Locate the cells, classifying each as a parasitized RBC, an uninfected RBC, or a WBC.
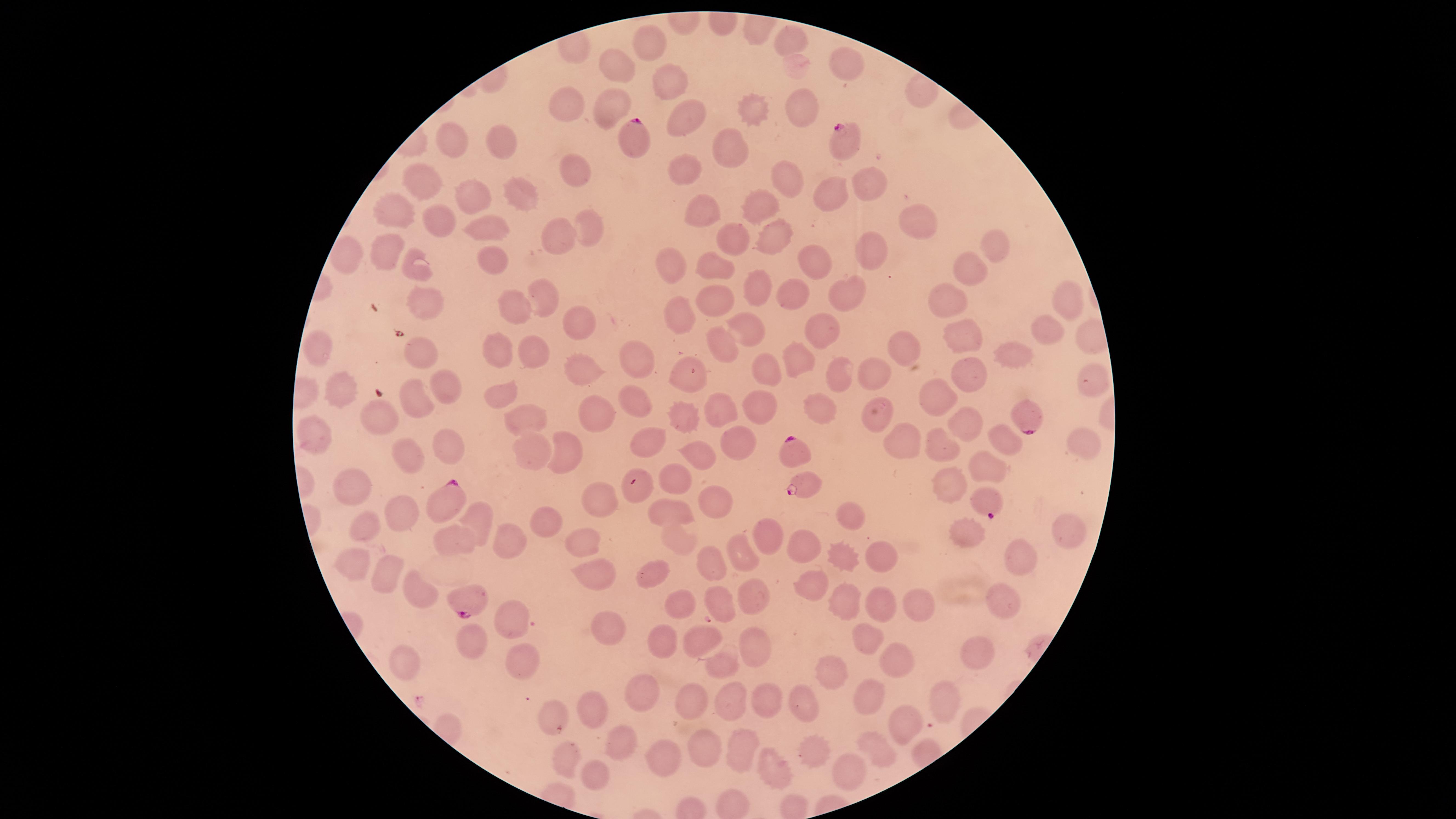

Approximate marker points as (x, y) in pixels.
Parasitized RBCs: (637, 140), (842, 140), (1023, 417), (793, 449), (805, 483), (633, 486), (449, 502), (988, 504), (472, 602).
Uninfected RBCs: (648, 41), (792, 43), (847, 66), (616, 68), (669, 85), (798, 105), (609, 106), (574, 107), (751, 113), (689, 117), (500, 135), (454, 142), (728, 151), (573, 170), (426, 173), (689, 173), (789, 173), (866, 181), (524, 189), (832, 196), (473, 201), (759, 204), (701, 208), (397, 214), (438, 216), (918, 218), (592, 223), (487, 230), (563, 230), (769, 239), (728, 242), (388, 251), (879, 251), (995, 251), (495, 259), (807, 260), (671, 262), (720, 266), (420, 267), (972, 270), (761, 284), (800, 292), (716, 295), (844, 295), (1063, 298), (548, 302), (420, 304), (506, 305), (945, 305), (677, 313), (579, 325), (819, 326), (751, 330), (1050, 332), (964, 338), (720, 342), (319, 348), (531, 349), (899, 350), (999, 351), (492, 352), (419, 353), (794, 363), (636, 364), (767, 368), (876, 371), (693, 372), (579, 374), (838, 374), (972, 376), (1083, 379), (340, 382), (439, 390), (499, 395), (415, 398), (759, 404), (941, 404), (632, 409), (822, 409), (377, 412), (723, 412), (877, 412), (685, 416), (526, 419), (975, 420), (595, 424), (310, 436), (646, 439), (950, 439), (903, 441), (569, 442), (1006, 443), (448, 447), (742, 447), (1083, 447), (530, 448), (706, 452), (399, 454), (985, 463), (680, 471), (956, 482), (355, 486), (600, 497), (714, 503), (670, 504), (404, 517), (855, 517), (545, 518), (481, 521), (366, 525), (970, 531), (1069, 535), (766, 538), (581, 540), (583, 542), (514, 544), (803, 544), (454, 546), (680, 546), (879, 554), (1017, 554), (352, 558), (744, 559), (843, 559), (711, 567), (383, 569), (650, 574), (598, 576), (808, 589), (415, 590), (750, 596), (717, 600), (876, 602), (915, 603), (679, 607), (992, 607), (844, 608), (508, 618), (602, 627), (703, 637), (871, 640), (473, 641), (754, 645), (662, 646), (973, 646), (400, 657), (895, 658), (520, 660), (725, 668), (836, 673), (640, 686), (876, 690), (941, 695), (690, 696), (759, 696), (734, 698), (808, 701), (594, 706), (552, 707), (904, 721), (625, 734), (705, 741), (736, 747), (819, 748), (874, 750), (566, 756), (660, 761), (849, 769), (774, 771), (597, 774).
No WBCs identified.

preparation = thin blood smear
visible region = circular
species = Plasmodium falciparum
image size = 1456×819 pixels
field of view = single
stain = Giemsa
capture = smartphone photograph through the microscope eyepiece